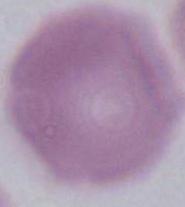

magnification = 1000x
identification = red blood cell
modality = photomicrograph